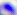

Summary:
  - Modality: photomicrograph
  - Identification: Toxoplasma gondii
  - Magnification: 400x